Assess this cell for malaria.
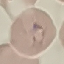

It is parasitized.

Summary:
  - Stain: Giemsa
  - Capture: smartphone camera at the microscope eyepiece
  - Preparation: thin smear
  - Image type: cell patch, automatically extracted from a larger field of view and resized to 64 × 64 pixels